Report the malaria status of this cell.
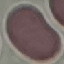

It is uninfected.

Acquired by smartphone through the microscope eyepiece. Thin blood film. Giemsa stain. Cell patch, automatically extracted from a larger field of view and resized to 64 × 64 pixels.